Describe the morphology of the erythrocytes.
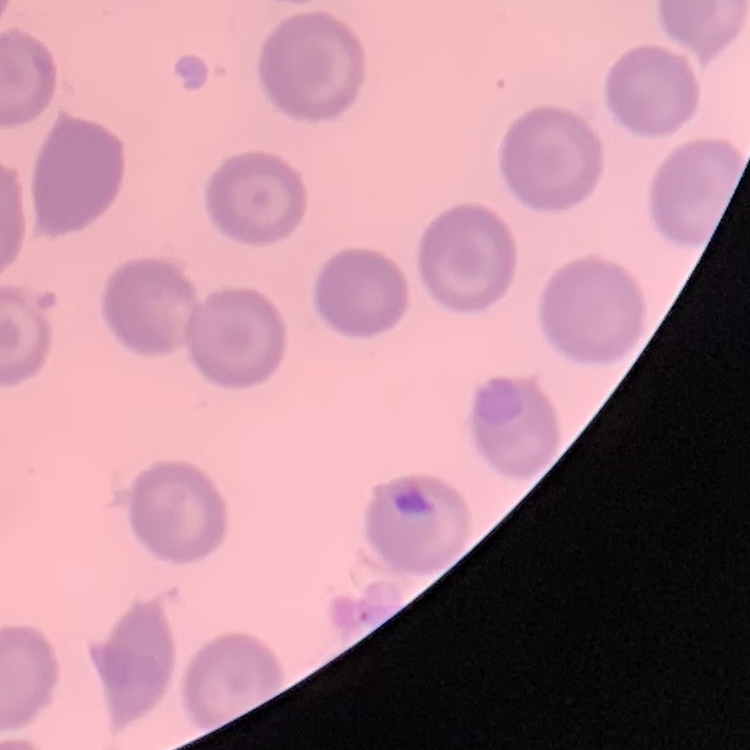
They show no rouleaux formation.

image_type: one tile cut from a larger photomicrograph
stain: Field's or Giemsa
preparation: thin blood film